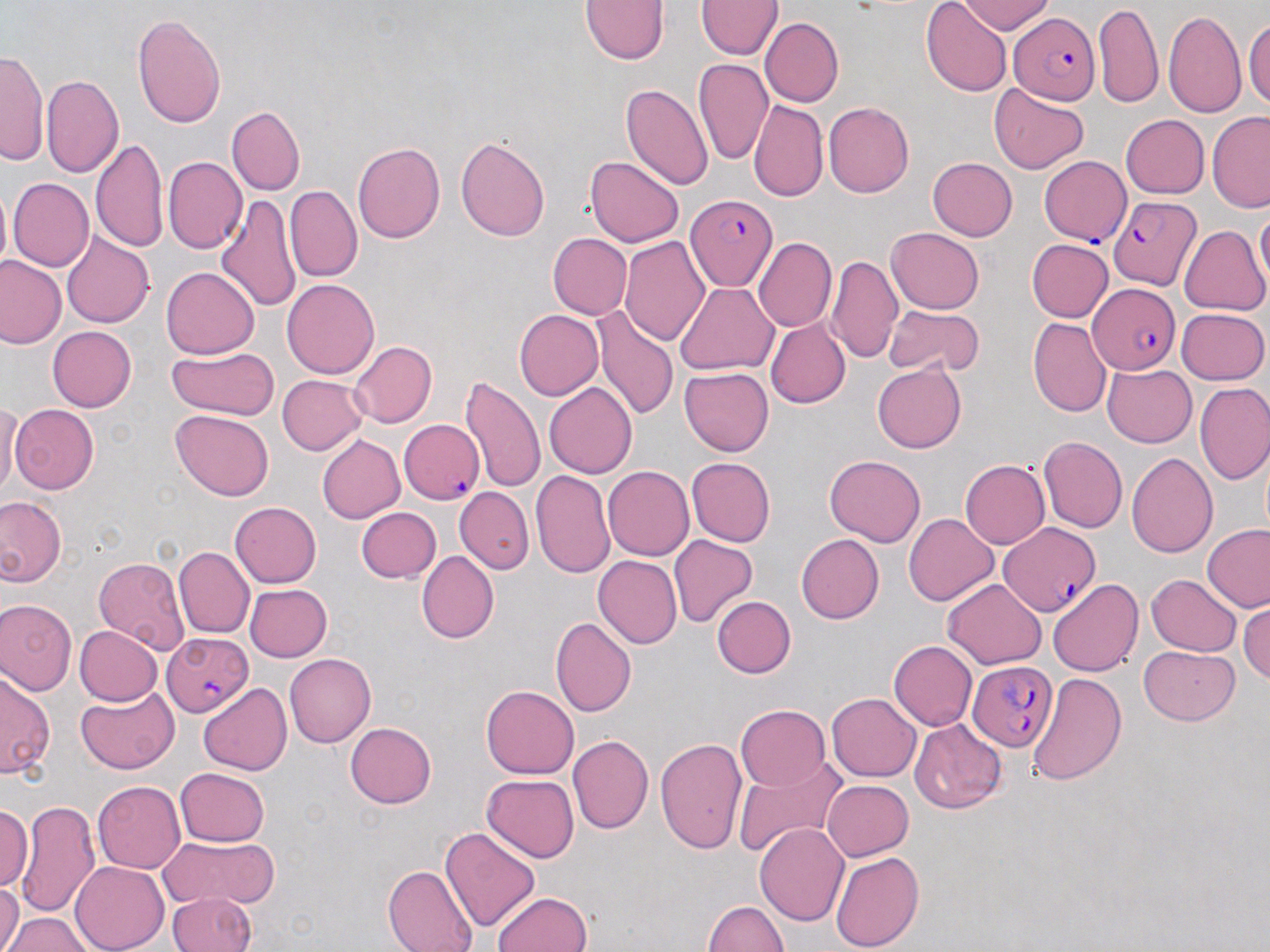

slide-level diagnosis = Plasmodium falciparum
image size = 1270×952 pixels
magnification = 1000x
field of view = single
preparation = thin blood smear
stain = May-Grünwald-Giemsa
modality = optical microscopy
Plasmodium falciparum-infected red blood cell locations = approximate bounding boxes as (x1, y1, x2, y2) in pixels: (1009, 13, 1098, 104), (1039, 156, 1132, 245), (685, 193, 780, 293), (1109, 195, 1202, 290), (1088, 283, 1180, 373), (398, 419, 484, 504), (998, 522, 1101, 617), (162, 632, 253, 716), (967, 660, 1058, 751)
uninfected red blood cell locations = approximate bounding boxes as (x1, y1, x2, y2) in pixels: (957, 0, 1056, 35), (579, 1, 668, 65), (696, 1, 782, 58), (921, 1, 1013, 98), (1093, 1, 1163, 108), (1163, 10, 1245, 118), (131, 13, 227, 129), (1244, 13, 1270, 112), (760, 17, 843, 107), (0, 49, 49, 166), (693, 58, 773, 166), (43, 74, 124, 177), (988, 81, 1089, 174), (622, 82, 713, 190), (749, 99, 828, 203), (824, 102, 914, 198), (226, 105, 304, 196), (1207, 110, 1270, 213), (1120, 114, 1209, 198), (456, 135, 550, 241), (91, 137, 168, 254), (353, 143, 445, 243), (162, 156, 247, 254), (585, 157, 683, 247), (927, 157, 1017, 240), (4, 177, 75, 349), (8, 178, 94, 271), (0, 183, 11, 279), (285, 185, 362, 283), (216, 194, 303, 314), (1255, 206, 1270, 292), (1179, 225, 1269, 315), (886, 227, 984, 314), (61, 232, 154, 328), (548, 233, 632, 319), (620, 236, 710, 345), (753, 238, 836, 332), (1026, 239, 1113, 322), (827, 254, 903, 364), (0, 257, 65, 349), (161, 266, 259, 359), (282, 279, 379, 379), (674, 282, 777, 376), (881, 303, 985, 377), (593, 306, 679, 421), (1177, 308, 1269, 384), (514, 309, 604, 400), (766, 318, 851, 409), (1028, 318, 1111, 418), (47, 326, 136, 412), (347, 341, 437, 428), (166, 346, 280, 420), (280, 355, 435, 440), (872, 363, 966, 453), (1103, 364, 1197, 447), (679, 367, 773, 455), (278, 375, 368, 455), (459, 376, 546, 493), (544, 382, 637, 480), (1195, 383, 1270, 484), (1, 404, 23, 497), (9, 404, 99, 494), (170, 410, 274, 501), (317, 434, 405, 524), (1038, 436, 1127, 533), (1127, 452, 1218, 558), (824, 456, 926, 547), (687, 458, 775, 547), (960, 459, 1050, 549), (602, 465, 695, 560), (530, 470, 615, 578), (455, 487, 534, 573), (0, 497, 65, 586), (230, 501, 321, 587), (356, 507, 441, 583), (903, 512, 998, 606), (1203, 524, 1270, 612), (796, 533, 884, 624), (668, 535, 758, 628), (173, 547, 255, 638), (416, 551, 498, 644), (593, 555, 682, 648), (94, 556, 190, 653), (1146, 574, 1242, 656), (942, 579, 1046, 669), (1049, 579, 1144, 677), (245, 584, 332, 662), (712, 596, 796, 678), (1, 599, 76, 694), (1239, 599, 1269, 685), (550, 617, 636, 719), (73, 626, 161, 706), (889, 640, 978, 731), (1140, 645, 1240, 725), (284, 653, 376, 748), (0, 670, 55, 779), (1029, 672, 1127, 785), (198, 684, 292, 775), (481, 684, 579, 779), (76, 687, 180, 772), (827, 693, 920, 781), (735, 704, 829, 790), (909, 718, 1007, 815), (345, 722, 436, 809), (568, 734, 653, 834), (654, 738, 749, 853), (733, 755, 847, 858), (176, 767, 269, 846), (482, 774, 579, 863), (822, 780, 913, 861), (91, 781, 186, 874), (15, 801, 99, 920), (0, 804, 33, 890), (754, 823, 849, 927), (439, 825, 540, 933), (158, 836, 280, 912), (830, 851, 925, 952), (71, 861, 169, 952), (381, 862, 478, 952), (0, 878, 23, 952), (491, 891, 593, 952), (166, 892, 256, 952), (700, 900, 788, 952), (0, 912, 97, 951)